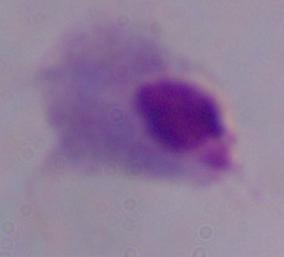

Photomicrograph. Captured at 1000x magnification. A trichomonad is seen.